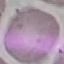

malaria status = uninfected
capture = smartphone through the microscope eyepiece
preparation = thin blood film
image type = cell patch, automatically extracted from a larger field of view and resized to 64 × 64 pixels
stain = Giemsa